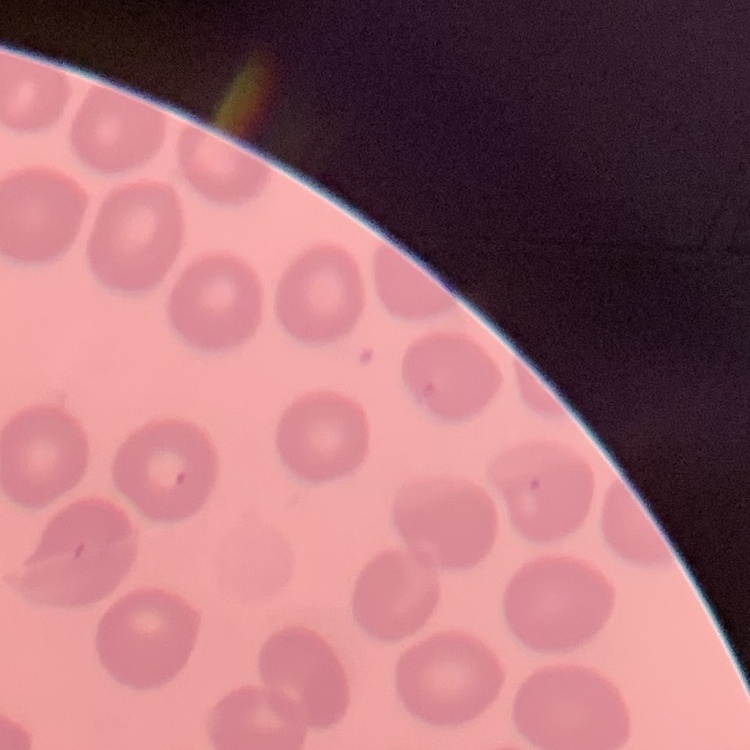
erythrocyte_morphology: no rouleaux formation
image_type: square crop of a larger photomicrograph
preparation: thin blood smear
stain: Field's or Giemsa